Outline each blood parasite and name the species.
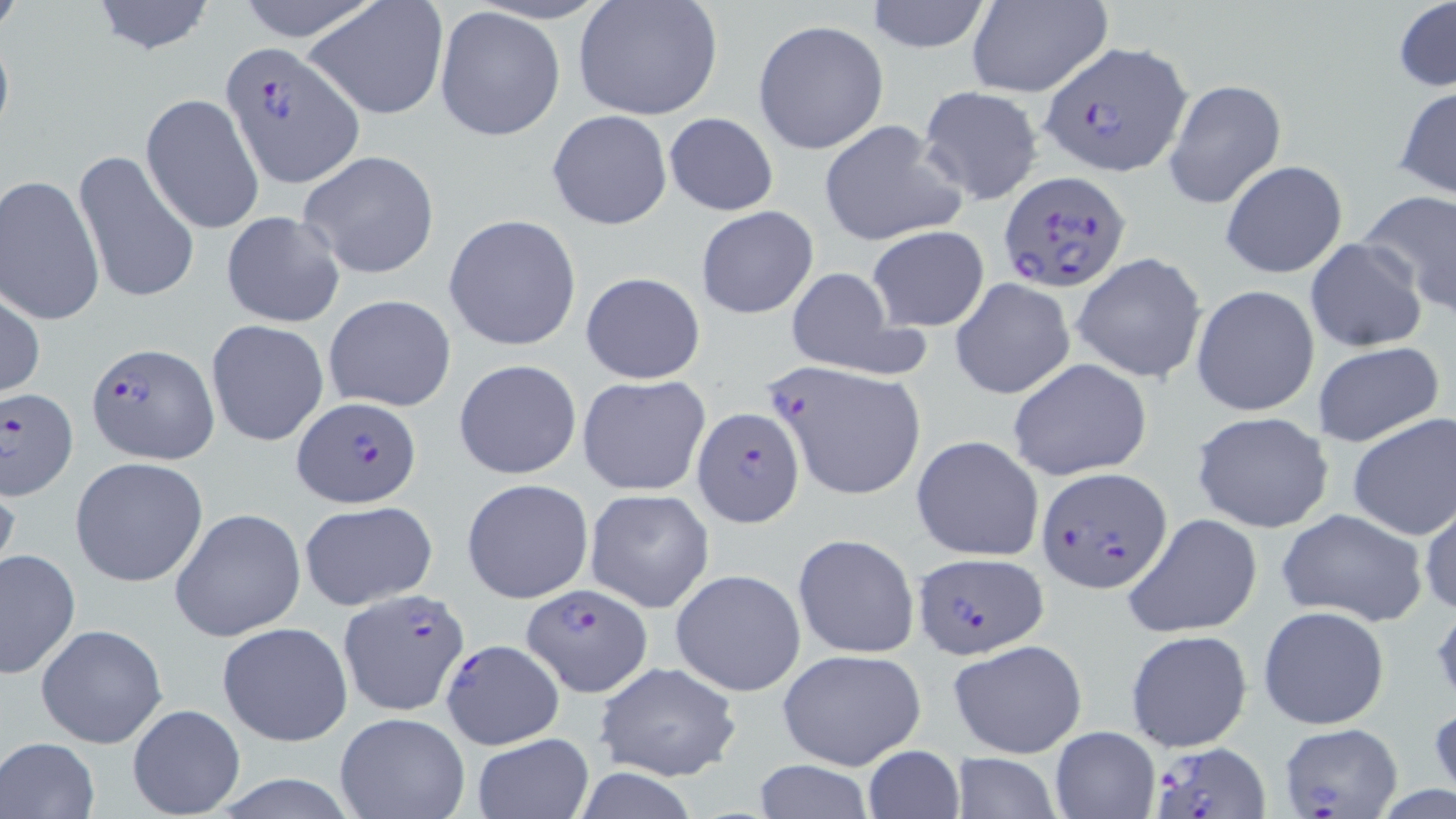
Approximate bounding boxes as [x1, y1, x2, y2] in pixels.
Plasmodium falciparum-infected red blood cells: [1038, 40, 1194, 177], [218, 42, 361, 187], [999, 169, 1133, 293], [87, 341, 217, 461], [0, 386, 79, 500], [293, 398, 420, 509], [693, 407, 805, 527], [1036, 466, 1170, 593], [910, 550, 1048, 658], [521, 581, 652, 695], [337, 590, 472, 716], [440, 637, 565, 750], [1278, 722, 1403, 815], [1152, 743, 1271, 819].
No Plasmodium ovale, Plasmodium malariae, Plasmodium vivax, Babesia divergens, or Trypanosoma brucei observed.

Summary:
  - Uninfected red blood cell locations: [88, 0, 216, 55], [234, 0, 383, 44], [305, 0, 450, 121], [574, 0, 723, 122], [865, 0, 993, 53], [1394, 0, 1456, 93], [968, 1, 1112, 97], [434, 5, 565, 141], [753, 19, 890, 156], [1164, 79, 1289, 210], [1393, 83, 1456, 200], [916, 84, 1045, 205], [141, 92, 266, 233], [547, 109, 673, 232], [663, 112, 779, 216], [817, 119, 969, 248], [73, 146, 200, 307], [298, 149, 440, 279], [1220, 160, 1348, 278], [1, 174, 105, 325], [1358, 191, 1456, 317], [695, 206, 819, 319], [219, 210, 346, 329], [444, 214, 582, 351], [866, 225, 990, 332], [1306, 238, 1426, 352], [1070, 252, 1207, 384], [784, 269, 910, 377], [580, 271, 706, 385], [950, 277, 1076, 400], [1192, 285, 1319, 417], [0, 290, 45, 400], [324, 295, 457, 411], [205, 319, 330, 448], [1313, 341, 1444, 448], [1008, 357, 1154, 481], [452, 358, 583, 481], [767, 359, 925, 499], [577, 374, 711, 496], [1190, 411, 1336, 534], [1347, 413, 1456, 540], [911, 435, 1044, 563], [69, 457, 209, 588], [0, 472, 22, 591], [461, 478, 594, 604], [584, 488, 714, 612], [1418, 495, 1456, 621], [299, 499, 438, 611], [1276, 507, 1429, 627], [170, 508, 304, 640], [1124, 514, 1262, 639], [793, 532, 919, 659], [0, 547, 81, 680], [669, 568, 806, 698], [1258, 604, 1390, 730], [216, 622, 352, 747], [36, 624, 168, 748], [1124, 629, 1253, 752], [947, 638, 1088, 758], [775, 647, 928, 770], [592, 663, 741, 782], [1428, 695, 1456, 800], [126, 703, 246, 817], [335, 709, 471, 818], [1051, 727, 1160, 818], [471, 733, 593, 818], [1, 736, 101, 818], [860, 745, 967, 819], [950, 753, 1059, 819], [751, 760, 876, 818]
  - Slide-level diagnosis: Plasmodium falciparum
  - Preparation: thin blood smear
  - Field of view: one of a larger specimen
  - Magnification: 1000x
  - Modality: light microscopy
  - Image size: 1456×819 pixels
  - Stain: May-Grünwald-Giemsa